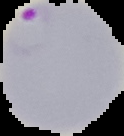
{
  "result": "malaria parasites detected",
  "image_type": "cell region segmented out of the field of view; surrounding area masked to black",
  "image_size": "124×136 pixels",
  "preparation": "thin blood smear"
}